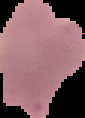

Summary:
  - Preparation: thin blood smear
  - Result: malaria parasites identified
  - Image size: 85×118 pixels
  - Image type: cell region segmented out of the field of view; surrounding area masked to black